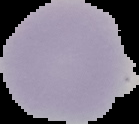

Summary:
  - Malaria status: uninfected
  - Preparation: thin blood smear
  - Image type: segmented cell region on a black background
  - Image size: 139×124 pixels